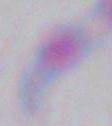

magnification = 1000x
identification = Toxoplasma gondii
modality = photomicrograph